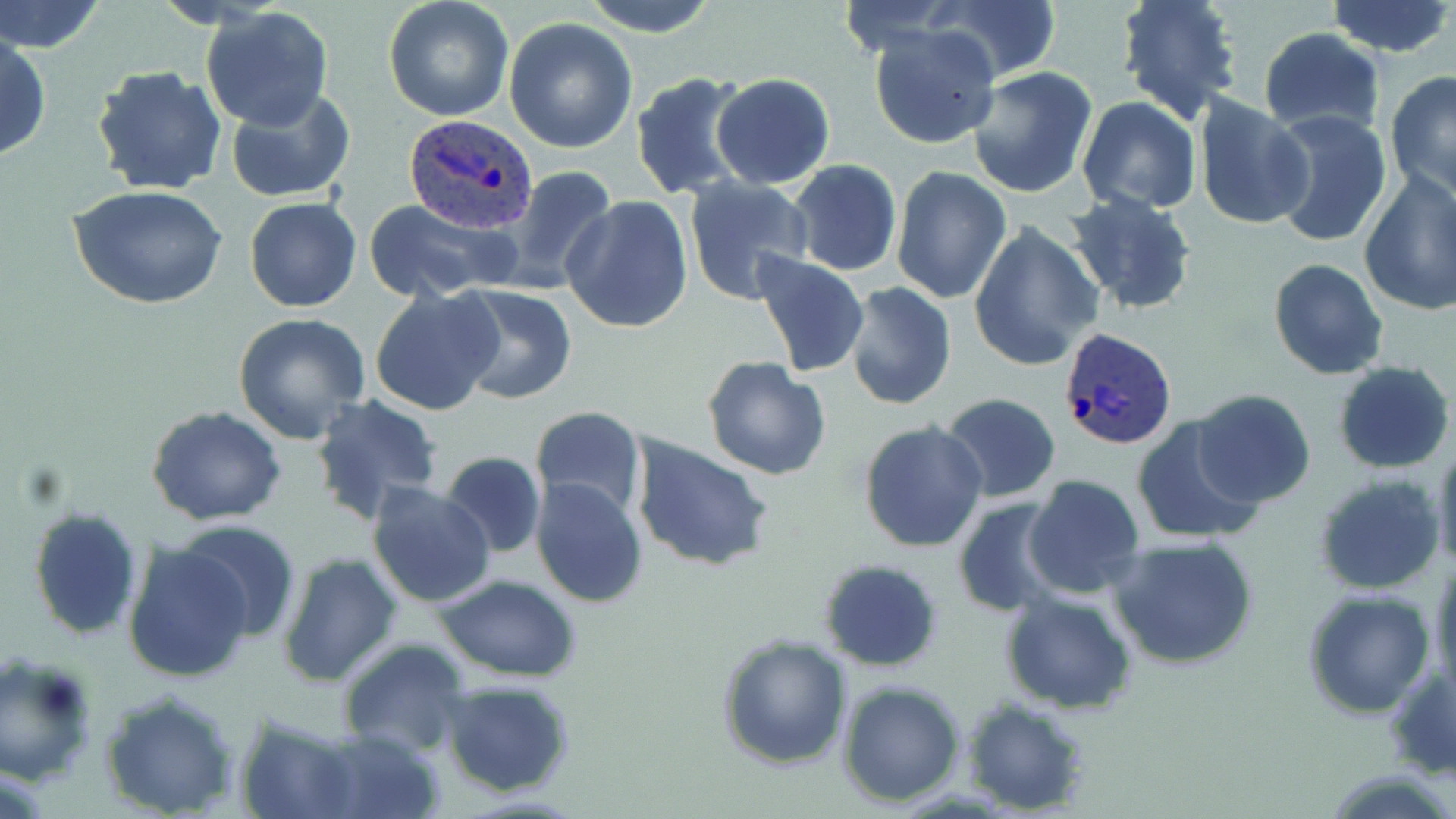

Summary:
  - Coordinate format: approximate bounding boxes as (x1, y1, x2, y2) in pixels
  - Uninfected red blood cell locations (subset): (0, 0, 108, 55), (383, 0, 513, 121), (576, 0, 723, 36), (933, 0, 1063, 84), (1325, 0, 1454, 58), (1116, 1, 1244, 124), (200, 7, 334, 132), (504, 18, 638, 155), (870, 25, 1003, 151), (1256, 26, 1386, 137), (0, 31, 51, 163), (91, 64, 227, 196), (966, 66, 1098, 197), (1384, 70, 1456, 198), (629, 71, 752, 201), (710, 72, 836, 189), (222, 86, 355, 204), (1192, 94, 1313, 231), (1076, 97, 1202, 216), (1268, 109, 1392, 250), (788, 160, 902, 277), (891, 165, 1012, 304), (494, 166, 618, 295), (1356, 169, 1456, 318), (682, 177, 814, 304), (67, 184, 227, 310), (1064, 190, 1200, 317), (560, 195, 694, 335), (244, 196, 360, 312), (362, 198, 516, 302), (968, 219, 1102, 371), (751, 248, 870, 380), (1268, 258, 1390, 381), (843, 283, 955, 409), (447, 284, 578, 405), (369, 287, 504, 417), (232, 313, 371, 444), (703, 356, 833, 479), (1332, 360, 1454, 474), (1191, 389, 1316, 508), (940, 392, 1061, 502), (310, 394, 444, 526), (146, 406, 286, 526), (530, 407, 647, 522), (1131, 416, 1264, 547), (859, 420, 989, 554), (629, 435, 773, 572), (1430, 445, 1456, 576), (441, 451, 545, 559), (1023, 474, 1146, 602), (531, 477, 648, 607), (366, 482, 496, 608), (952, 497, 1065, 618), (27, 506, 143, 641), (179, 523, 301, 642), (1109, 535, 1259, 671), (123, 541, 255, 683), (277, 553, 404, 686), (1428, 558, 1456, 698), (818, 559, 946, 673), (431, 572, 583, 681), (1301, 588, 1437, 716), (1001, 594, 1138, 714), (716, 632, 852, 770), (337, 636, 470, 757), (0, 653, 101, 787), (1384, 661, 1456, 780), (439, 676, 576, 799), (838, 680, 966, 806), (98, 687, 241, 818), (959, 696, 1092, 816), (235, 712, 364, 819), (312, 728, 445, 819)
  - Plasmodium ovale-infected red blood cell locations (subset): (402, 115, 541, 236), (1058, 328, 1177, 452)
  - Slide-level diagnosis: Plasmodium ovale
  - Field of view: single
  - Preparation: thin blood film
  - Magnification: 1000x
  - Image size: 1456×819 pixels
  - Modality: light microscopy
  - Stain: May-Grünwald-Giemsa